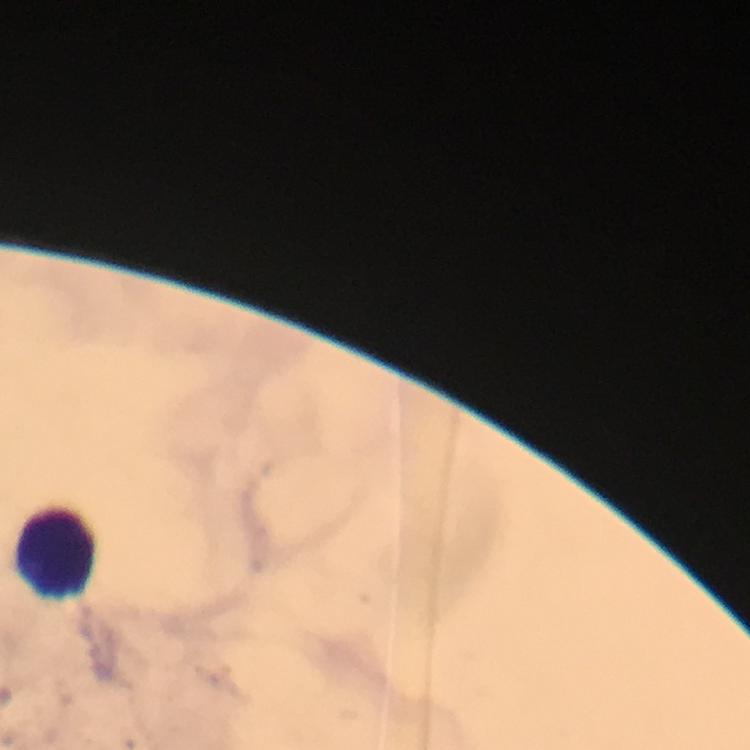

Approximate centers as (x, y) in pixels. Leukocyte locations: (54, 556). Thick smear. Malaria parasites: none detected. From a diagnostic examination for malaria. A crop from one field of view. At 100x magnification. Immersion oil applied. Giemsa-stained preparation. Photographed with a smartphone mounted on the microscope. Image is 750×750 pixels.